Outline each Plasmodium falciparum parasite and classify it by life-cycle stage.
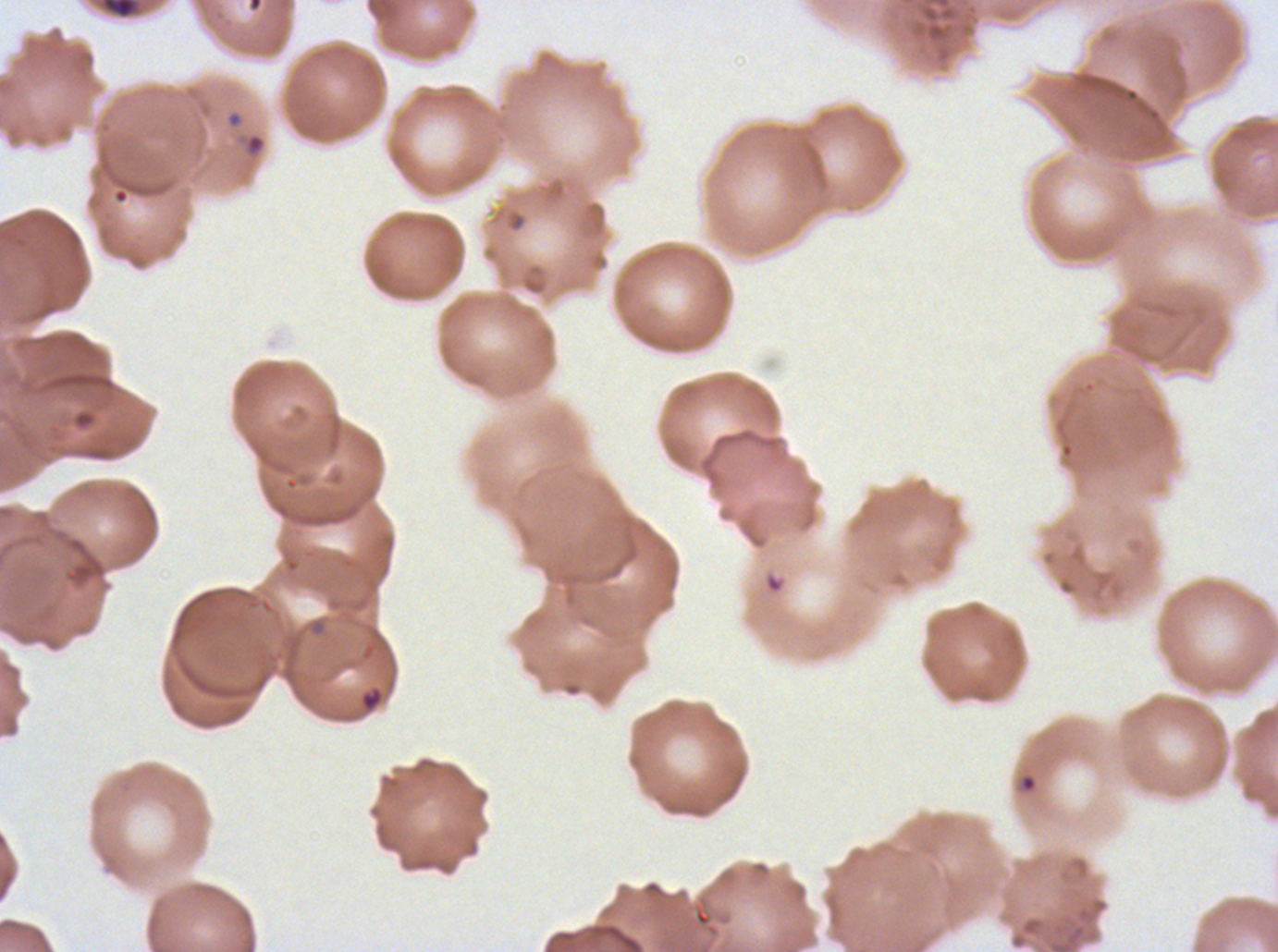

Approximate bounding boxes as [x1, y1, x2, y2] in pixels.
Rings: [245, 133, 265, 155], [359, 686, 384, 712].
No late-ring/early-trophozoite forms, mid trophozoites, late trophozoites, early schizonts, late schizonts, segmenters, or gametocytes observed.

{
  "image_size": "1278×952 pixels",
  "preparation": "thin blood smear",
  "debris_locations": "approximate bounding boxes as [x1, y1, x2, y2] in pixels: [100, 0, 141, 19]",
  "field_of_view": "one sub-image of a larger composite",
  "specimen": "Plasmodium falciparum from a patient in The Gambia, cultured ex vivo for 24 to 48 hours",
  "stain": "Giemsa"
}